Locate every blood parasite and identify its species.
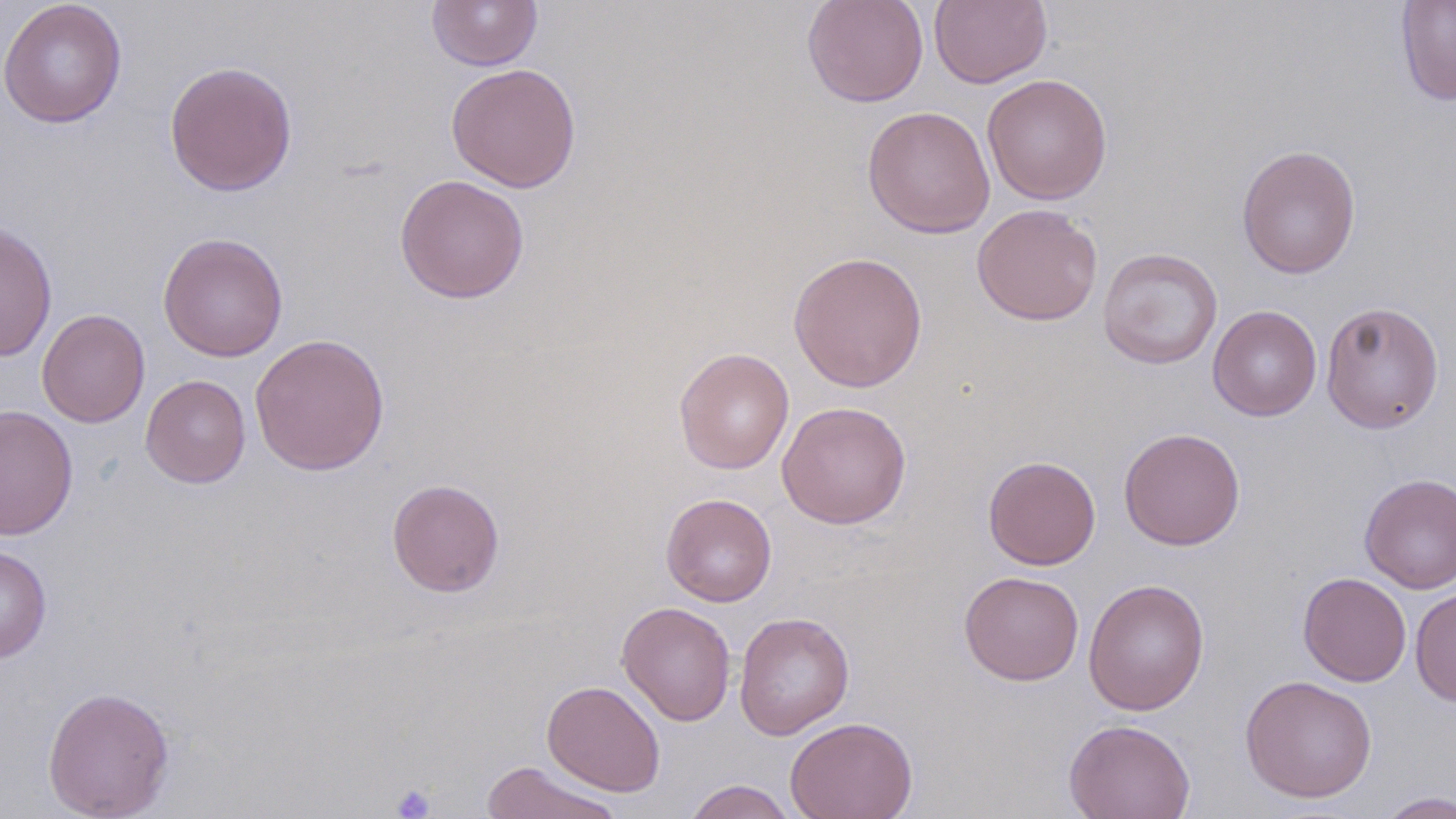

No blood parasites seen.

Summary:
  - Coordinate format: approximate bounding boxes as (x1,y1)-(x2,y2) corner pairs in pixels
  - Uninfected red blood cell locations: (0,0)-(127,129), (427,0)-(542,71), (801,0)-(929,108), (929,0)-(1053,89), (1396,0)-(1456,106), (164,60)-(298,197), (445,62)-(582,193), (982,73)-(1112,205), (862,105)-(995,239), (1236,144)-(1362,280), (394,174)-(530,304), (972,203)-(1104,325), (1,222)-(58,362), (157,232)-(288,362), (1097,248)-(1223,370), (787,250)-(928,393), (1320,301)-(1444,434), (1208,305)-(1322,422), (37,308)-(150,428), (250,333)-(390,475), (674,347)-(794,474), (140,375)-(251,488), (776,400)-(912,530), (0,404)-(78,540), (1118,427)-(1245,551), (983,455)-(1101,570), (1359,473)-(1456,593), (386,479)-(505,597), (660,493)-(777,607), (0,545)-(52,663), (958,570)-(1084,686), (1298,572)-(1411,686), (1083,578)-(1210,715), (1410,587)-(1456,707), (617,602)-(736,726), (734,611)-(854,740), (1240,674)-(1378,803), (542,679)-(665,796), (42,686)-(176,819), (785,716)-(918,819), (1064,718)-(1196,819), (479,761)-(626,819), (682,779)-(799,819), (1375,790)-(1456,818)
  - Platelet locations: (390,783)-(436,818)
  - Slide-level diagnosis: negative for blood parasites
  - Field of view: single
  - Stain: May-Grünwald-Giemsa
  - Magnification: 1000x
  - Modality: optical microscopy
  - Preparation: thin blood film
  - Image size: 1456×819 pixels